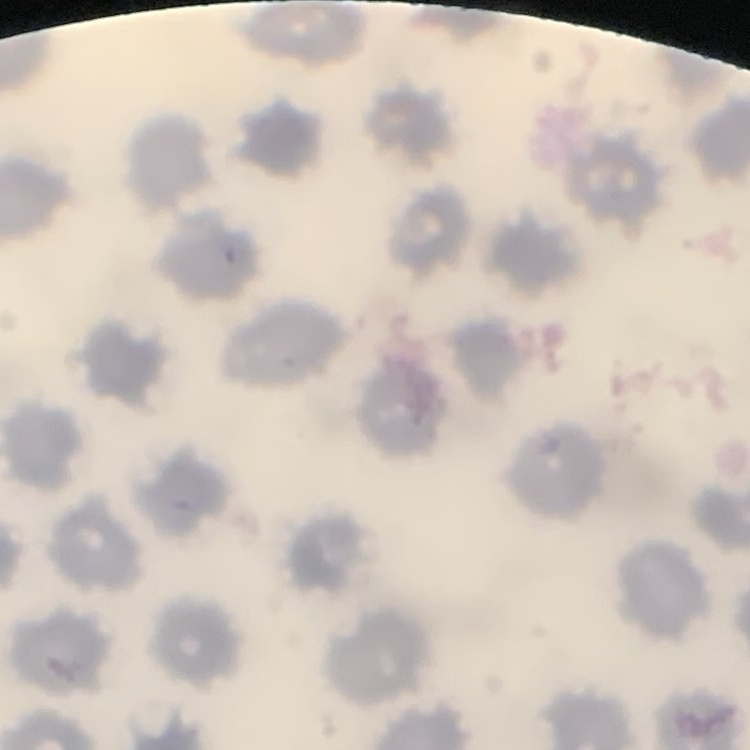

Summary:
  - Red blood cell morphology: no rouleaux formation
  - Preparation: thin peripheral smear
  - Image type: square crop of a larger photomicrograph
  - Stain: Field's or Giemsa